Describe the morphology of the erythrocytes.
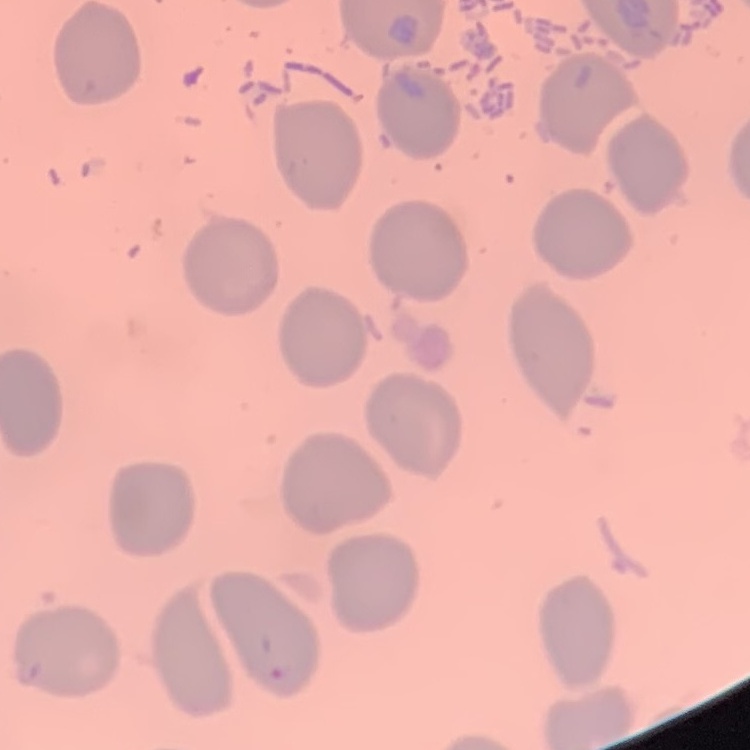

No rouleaux formation.

Thin peripheral smear. Stained with either Field's or Giemsa. Square crop of a larger photomicrograph.